Give a bounding box for every leukocyte visible.
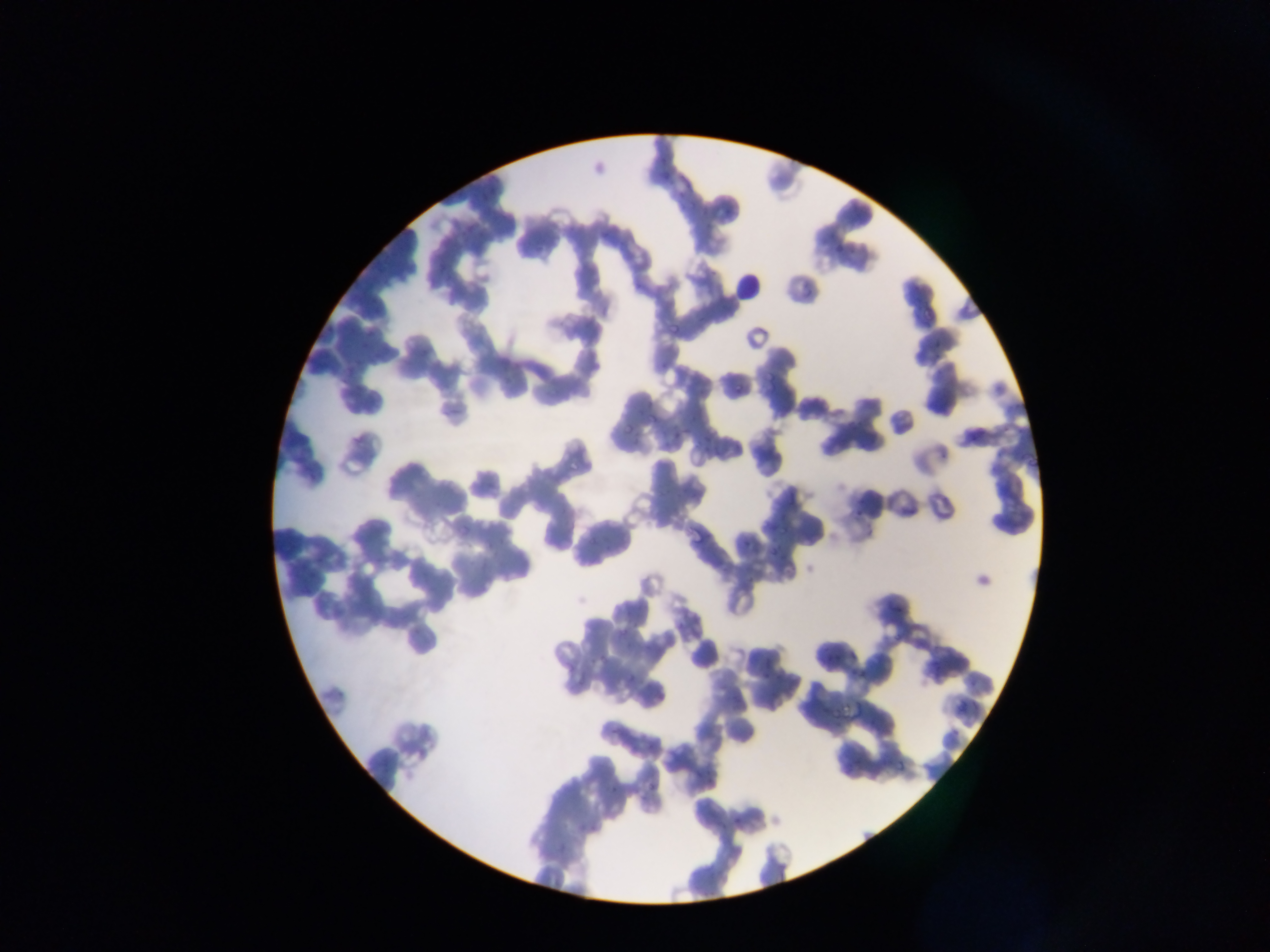
No leukocytes observed.

Approximate bounding boxes as {left, top, right, bottom} in pixels. Malaria parasite locations: {834, 247, 844, 254}, {805, 287, 813, 297}, {936, 342, 944, 349}, {936, 351, 942, 362}, {660, 361, 669, 367}, {735, 380, 741, 393}, {647, 413, 658, 426}, {623, 423, 633, 434}, {1003, 426, 1011, 433}, {1017, 430, 1029, 434}, {969, 436, 980, 442}, {993, 449, 1009, 459}, {941, 452, 950, 458}, {567, 462, 578, 472}, {855, 498, 864, 507}, {852, 511, 865, 520}, {743, 537, 754, 547}, {771, 544, 781, 555}, {892, 601, 903, 612}, {894, 622, 905, 637}, {620, 627, 631, 641}, {850, 648, 861, 658}, {827, 651, 834, 660}, {836, 654, 845, 660}, {589, 655, 600, 665}, {599, 655, 607, 661}, {932, 657, 943, 668}, {849, 667, 860, 676}, {762, 670, 770, 679}, {861, 670, 867, 678}, {625, 675, 635, 683}. Thin blood film. Image is 1270×952 pixels. Photographed through a microscope with a mobile-phone camera. Single field of view. Collected in Ghana.